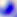 Photomicrograph. Toxoplasma gondii is shown. 400x magnification.